Describe the morphology of the red blood cells.
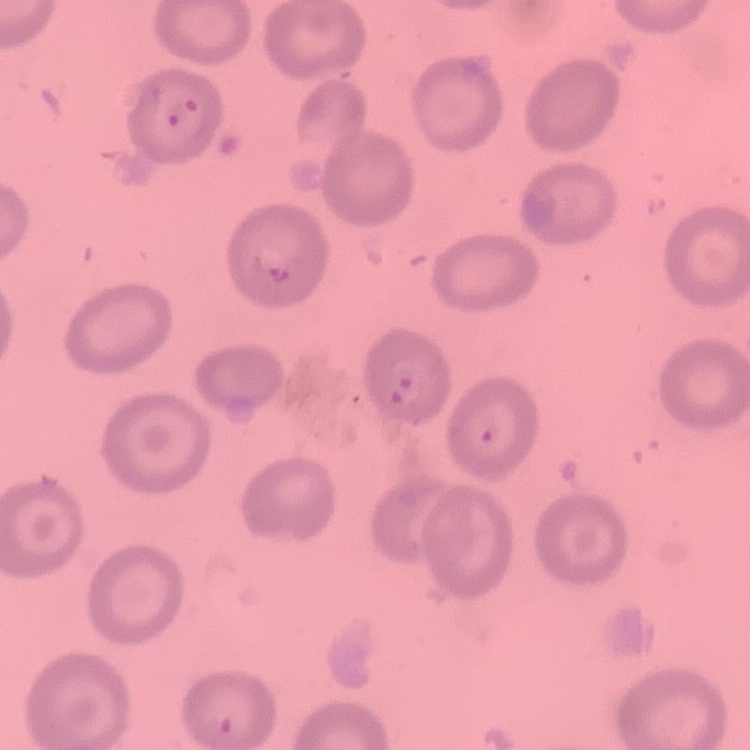

They show no rouleaux formation.

Summary:
  - Preparation: thin peripheral smear
  - Image type: square crop of a larger photomicrograph
  - Stain: Field's or Giemsa